Describe the morphology of the red blood cells.
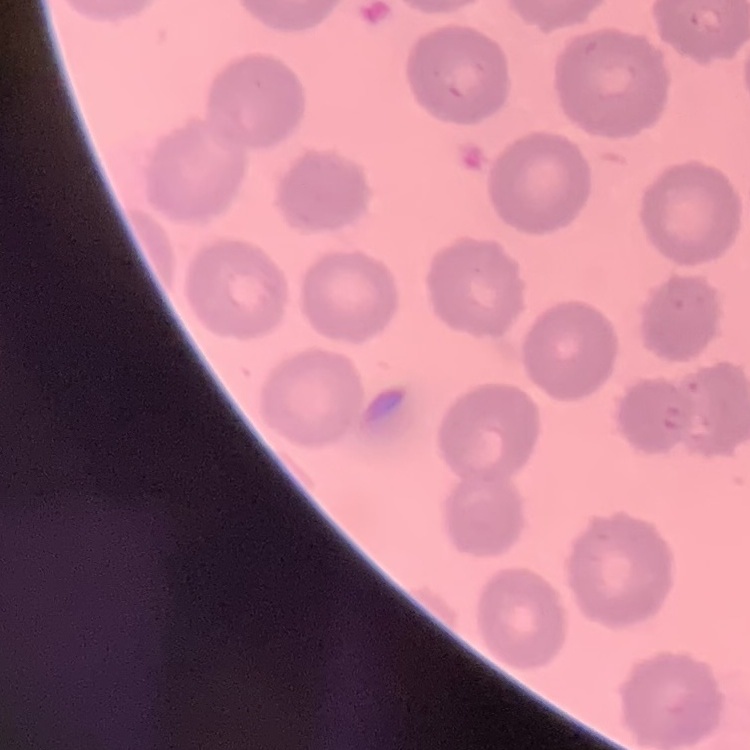

They show no rouleaux formation.

Summary:
  - Preparation: thin peripheral smear
  - Stain: Field's or Giemsa
  - Image type: square crop of a larger photomicrograph